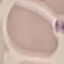

Summary:
  - Malaria status: uninfected
  - Image type: cell patch, automatically extracted from a larger field of view and resized to 64 × 64 pixels
  - Capture: smartphone camera at the microscope eyepiece
  - Preparation: thin blood film
  - Stain: Giemsa